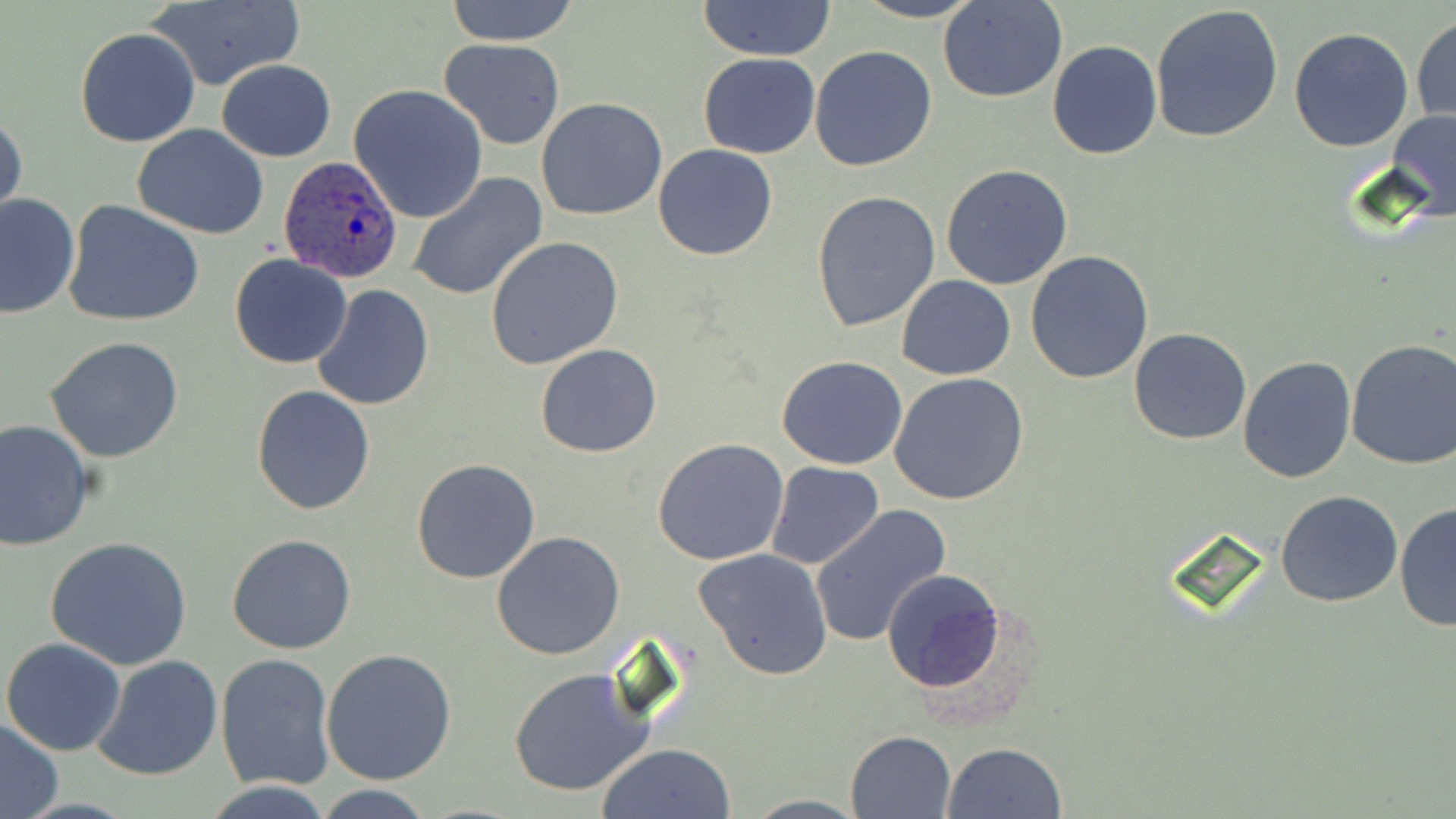 Approximate bounding boxes as (x1, y1, x2, y2) in pixels. Plasmodium ovale-infected red blood cell locations: (279, 155, 403, 283). Uninfected red blood cell locations: (445, 0, 580, 45), (851, 0, 985, 23), (144, 1, 304, 91), (696, 1, 838, 59), (939, 1, 1068, 103), (1150, 4, 1285, 144), (1411, 14, 1455, 125), (75, 26, 202, 148), (1289, 26, 1415, 152), (439, 37, 566, 149), (1047, 40, 1162, 159), (809, 45, 939, 173), (697, 52, 820, 158), (216, 59, 336, 161), (348, 84, 488, 223), (536, 97, 667, 220), (1387, 109, 1456, 222), (0, 110, 26, 229), (132, 124, 271, 239), (652, 143, 779, 260), (939, 163, 1073, 288), (406, 174, 547, 301), (810, 190, 942, 332), (1, 192, 81, 319), (64, 199, 204, 328), (485, 237, 625, 371), (1024, 250, 1154, 384), (229, 254, 353, 369), (896, 275, 1016, 380), (312, 284, 434, 411), (1128, 328, 1253, 445), (45, 337, 186, 464), (1344, 339, 1456, 470), (535, 345, 661, 459), (777, 355, 909, 471), (1238, 355, 1358, 484), (889, 373, 1029, 507), (251, 384, 377, 515), (0, 419, 93, 554), (652, 439, 790, 566), (411, 458, 541, 585), (766, 462, 884, 569), (1275, 489, 1402, 606), (1396, 501, 1455, 634), (809, 505, 950, 648), (491, 532, 626, 660), (227, 533, 358, 655), (46, 535, 193, 670), (695, 550, 834, 682), (882, 570, 1006, 693), (2, 637, 126, 756), (321, 647, 456, 785), (215, 653, 336, 790), (91, 654, 224, 780), (508, 668, 655, 798), (0, 719, 64, 818), (845, 731, 956, 819), (595, 743, 735, 819), (943, 743, 1067, 819), (200, 782, 336, 818), (314, 786, 435, 818), (741, 794, 866, 817). Slide-level diagnosis: Plasmodium ovale. May-Grünwald-Giemsa-stained preparation. Thin blood smear. Captured at 1000x magnification. One field of a larger specimen. Light microscopy. Image is 1456×819 pixels.